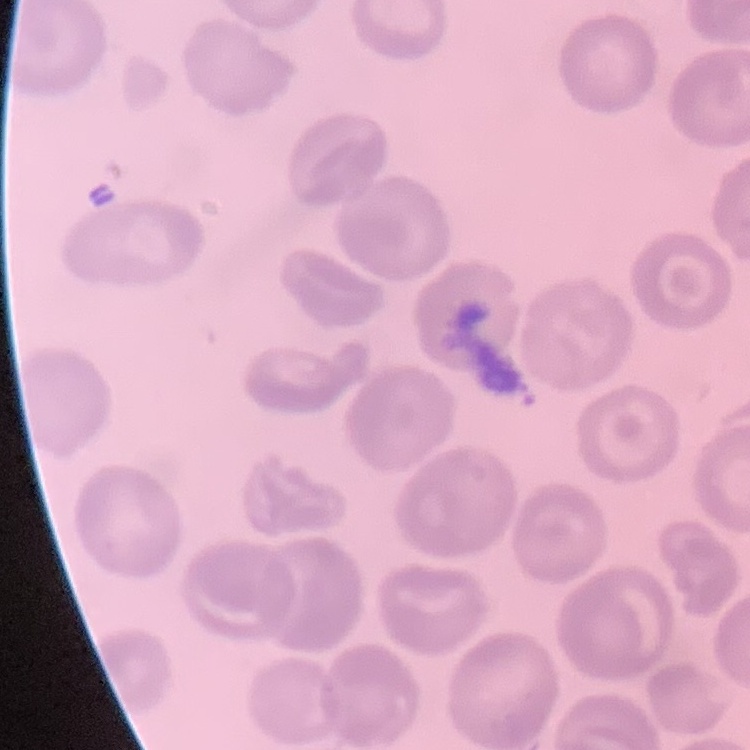
Summary:
  - Erythrocyte morphology: no rouleaux formation
  - Stain: Field's or Giemsa
  - Preparation: thin blood film
  - Image type: one tile cut from a larger photomicrograph